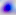
magnification: 400x
modality: photomicrograph
identification: Toxoplasma gondii